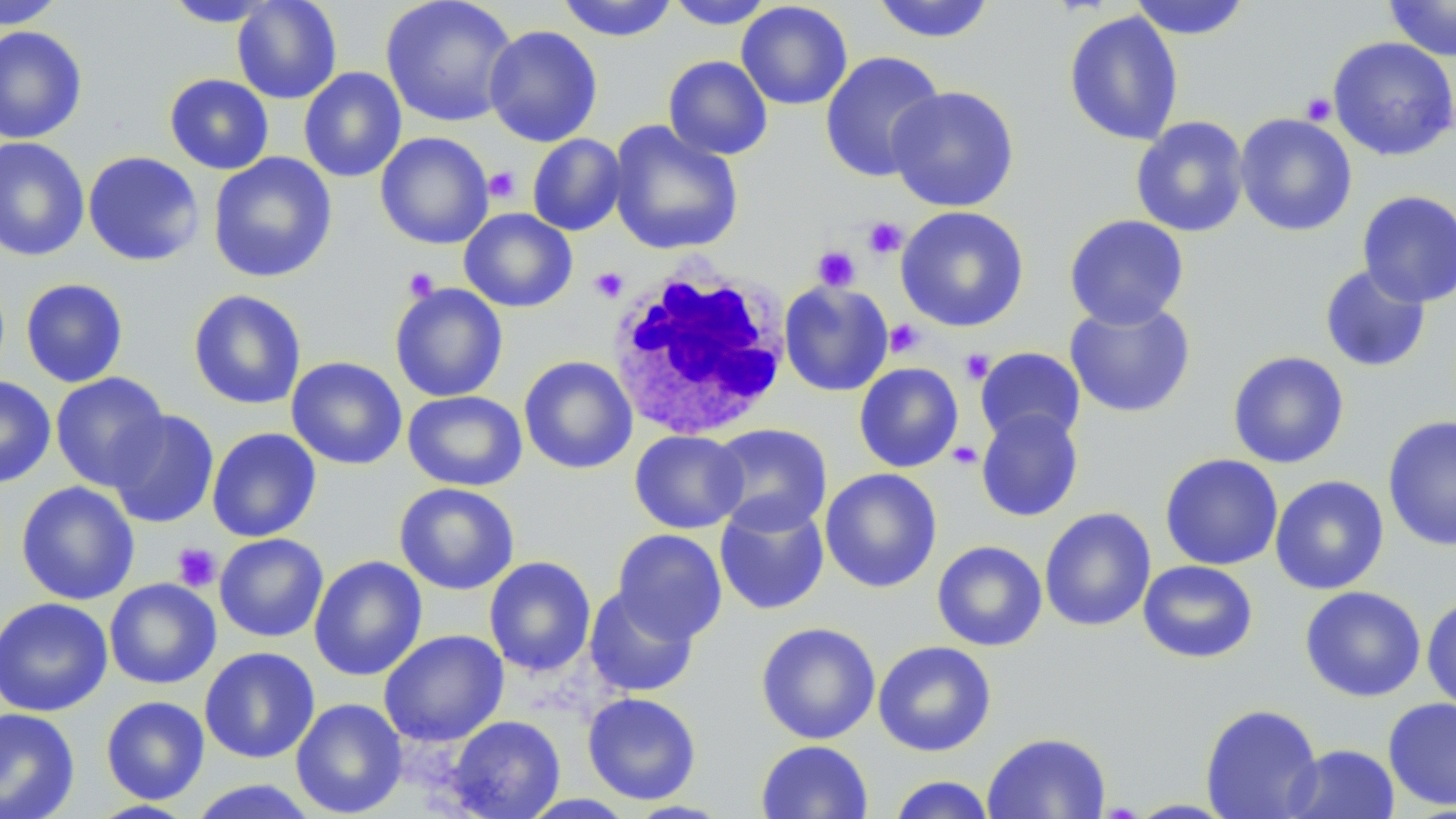

Approximate bounding boxes as named x1/y1/x2/y2 corners in pixels. White blood cell locations: (x1=606, y1=260, x2=792, y2=441). Uninfected red blood cell locations: (x1=0, y1=0, x2=67, y2=29), (x1=232, y1=0, x2=342, y2=104), (x1=380, y1=0, x2=518, y2=127), (x1=557, y1=0, x2=678, y2=42), (x1=870, y1=0, x2=997, y2=44), (x1=1383, y1=0, x2=1456, y2=61), (x1=163, y1=1, x2=279, y2=27), (x1=664, y1=1, x2=777, y2=29), (x1=1128, y1=1, x2=1252, y2=40), (x1=736, y1=2, x2=853, y2=110), (x1=1063, y1=10, x2=1184, y2=146), (x1=0, y1=25, x2=87, y2=144), (x1=483, y1=25, x2=602, y2=147), (x1=1328, y1=36, x2=1456, y2=162), (x1=820, y1=50, x2=945, y2=183), (x1=663, y1=55, x2=773, y2=160), (x1=298, y1=67, x2=407, y2=183), (x1=164, y1=74, x2=274, y2=175), (x1=886, y1=85, x2=1020, y2=213), (x1=1234, y1=113, x2=1357, y2=237), (x1=1131, y1=116, x2=1250, y2=238), (x1=607, y1=121, x2=744, y2=257), (x1=375, y1=132, x2=494, y2=250), (x1=527, y1=133, x2=627, y2=236), (x1=0, y1=137, x2=90, y2=262), (x1=83, y1=151, x2=205, y2=267), (x1=208, y1=153, x2=338, y2=283), (x1=1357, y1=190, x2=1455, y2=307), (x1=896, y1=205, x2=1030, y2=332), (x1=459, y1=208, x2=577, y2=313), (x1=1064, y1=214, x2=1189, y2=330), (x1=1319, y1=264, x2=1431, y2=373), (x1=20, y1=278, x2=128, y2=388), (x1=778, y1=280, x2=893, y2=396), (x1=390, y1=283, x2=508, y2=402), (x1=188, y1=289, x2=307, y2=410), (x1=1065, y1=300, x2=1196, y2=418), (x1=975, y1=347, x2=1086, y2=448), (x1=1227, y1=351, x2=1349, y2=469), (x1=286, y1=356, x2=407, y2=470), (x1=519, y1=356, x2=637, y2=474), (x1=854, y1=362, x2=963, y2=473), (x1=50, y1=372, x2=171, y2=491), (x1=0, y1=376, x2=56, y2=488), (x1=403, y1=390, x2=527, y2=492), (x1=975, y1=408, x2=1084, y2=522), (x1=106, y1=409, x2=219, y2=528), (x1=1383, y1=415, x2=1456, y2=552), (x1=708, y1=423, x2=832, y2=535), (x1=207, y1=427, x2=321, y2=542), (x1=629, y1=430, x2=748, y2=534), (x1=1159, y1=453, x2=1283, y2=570), (x1=820, y1=468, x2=942, y2=593), (x1=1270, y1=475, x2=1390, y2=595), (x1=15, y1=482, x2=140, y2=605), (x1=394, y1=482, x2=519, y2=595), (x1=714, y1=499, x2=830, y2=615), (x1=1039, y1=507, x2=1156, y2=632), (x1=612, y1=529, x2=727, y2=643), (x1=214, y1=533, x2=328, y2=642), (x1=932, y1=540, x2=1047, y2=652), (x1=309, y1=555, x2=428, y2=681), (x1=484, y1=556, x2=596, y2=677), (x1=1138, y1=560, x2=1258, y2=663), (x1=104, y1=578, x2=221, y2=689), (x1=583, y1=586, x2=700, y2=698), (x1=1300, y1=586, x2=1426, y2=702), (x1=1421, y1=595, x2=1456, y2=714), (x1=0, y1=597, x2=112, y2=716), (x1=755, y1=622, x2=881, y2=744), (x1=379, y1=629, x2=508, y2=746), (x1=873, y1=640, x2=997, y2=756), (x1=199, y1=647, x2=320, y2=763), (x1=581, y1=692, x2=702, y2=804), (x1=101, y1=695, x2=210, y2=804), (x1=1382, y1=696, x2=1456, y2=811), (x1=291, y1=698, x2=408, y2=818), (x1=1200, y1=703, x2=1323, y2=819), (x1=0, y1=708, x2=80, y2=819), (x1=447, y1=715, x2=565, y2=819), (x1=982, y1=732, x2=1111, y2=819), (x1=756, y1=740, x2=873, y2=819), (x1=1283, y1=743, x2=1400, y2=819), (x1=887, y1=775, x2=996, y2=819), (x1=186, y1=780, x2=321, y2=818), (x1=87, y1=800, x2=199, y2=818). Platelet locations: (x1=1300, y1=92, x2=1337, y2=126), (x1=484, y1=167, x2=520, y2=203), (x1=864, y1=217, x2=907, y2=258), (x1=812, y1=245, x2=861, y2=291), (x1=589, y1=267, x2=629, y2=303), (x1=403, y1=268, x2=439, y2=301), (x1=884, y1=320, x2=925, y2=358), (x1=960, y1=349, x2=994, y2=384), (x1=947, y1=441, x2=983, y2=470), (x1=172, y1=542, x2=221, y2=592). Slide-level diagnosis: no evidence of blood parasites. May-Grünwald-Giemsa-stained preparation. Single field of view. Optical microscopy. Image is 1456×819 pixels. Captured at 1000x magnification. Thin blood smear.